Point out each malaria parasite and each leukocyte.
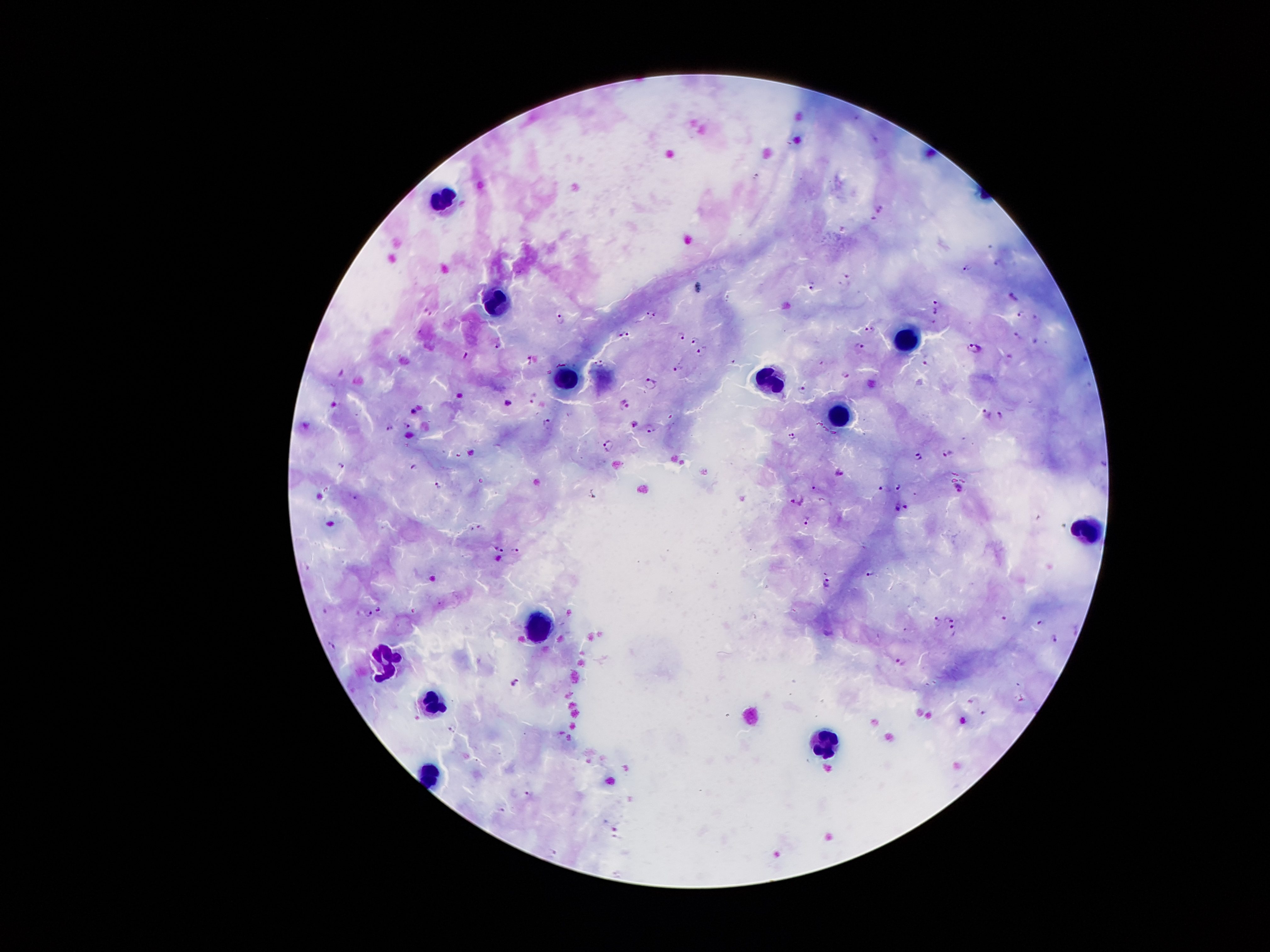
Approximate centers as [x, y] in pixels.
Malaria parasites: [881, 210], [996, 262], [967, 269], [844, 275], [811, 286], [1012, 295], [937, 307], [428, 308], [651, 312], [1022, 313], [560, 320], [933, 321], [872, 330], [623, 335], [1016, 335], [679, 336], [1033, 337], [694, 340], [498, 344], [860, 346], [974, 348], [701, 349], [465, 357], [527, 359], [732, 359], [926, 360], [598, 362], [676, 368], [846, 375], [650, 384], [800, 388], [533, 396], [625, 405], [414, 408], [987, 413], [1001, 414], [547, 421], [631, 423], [389, 425], [407, 425], [650, 428], [793, 437], [608, 446], [950, 453], [916, 455], [342, 463], [413, 464], [839, 473], [437, 484], [898, 487], [959, 487], [814, 490], [885, 490], [353, 497], [797, 499], [906, 506], [898, 508], [805, 519], [482, 528], [500, 549], [516, 549], [871, 573], [827, 582], [379, 607], [368, 613], [1003, 617], [936, 619], [949, 619], [1038, 620], [952, 629], [1053, 637], [334, 645], [901, 662], [513, 681], [983, 713], [528, 794].
Leukocytes: [446, 203], [495, 302], [913, 340], [771, 380], [565, 388], [839, 419], [1085, 529], [539, 627], [385, 656], [432, 704], [826, 744], [429, 777].

{
  "field_of_view": "single",
  "patient_malaria_status": "positive for Plasmodium falciparum",
  "magnification": "100x",
  "image_size": "1270×952 pixels",
  "stain": "Giemsa",
  "preparation": "thick blood smear",
  "capture": "smartphone through the microscope eyepiece"
}